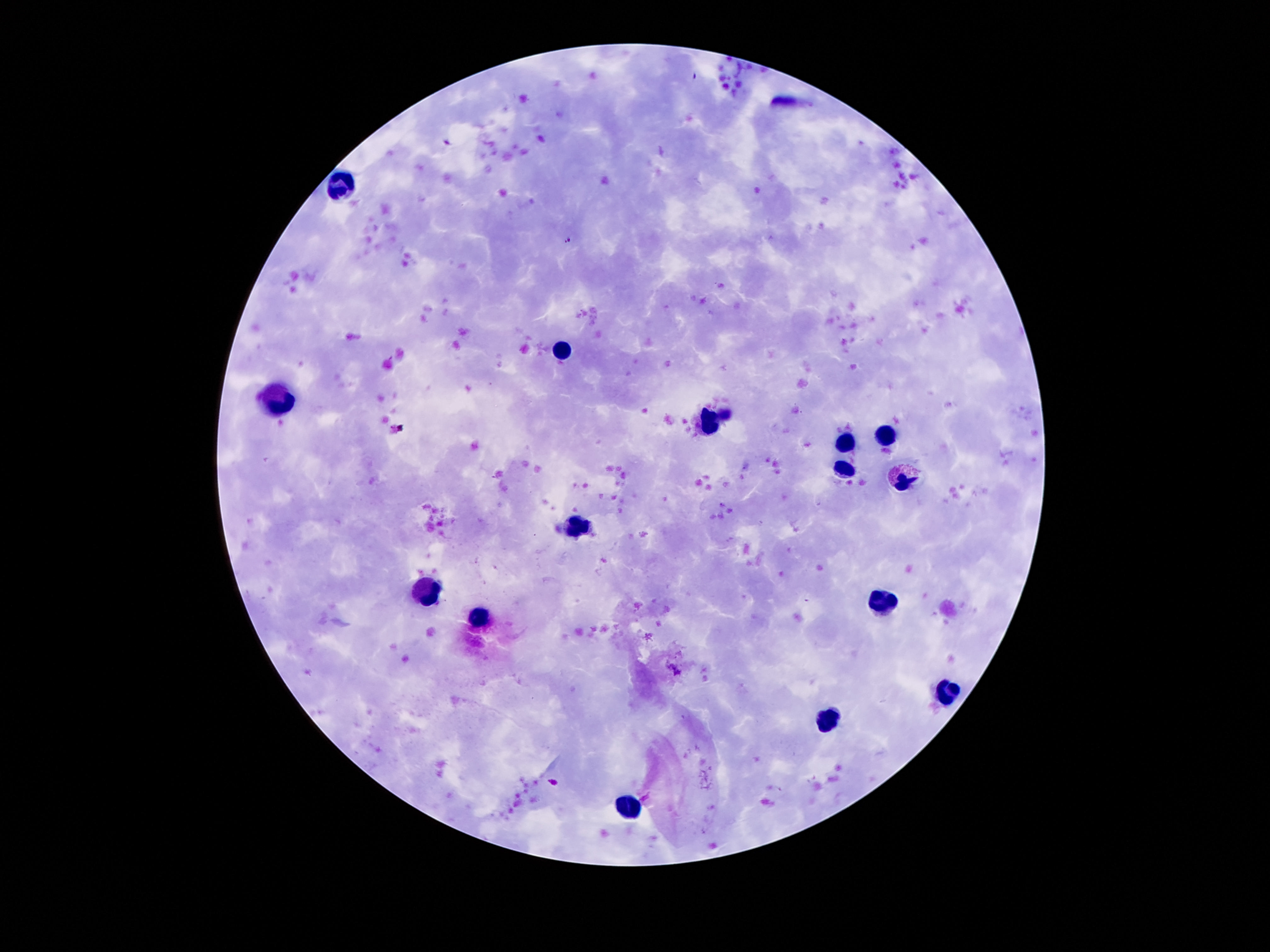
Approximate centers as {x, y} in pixels.
Summary:
  - Leukocyte locations: {343, 184}, {563, 347}, {274, 401}, {712, 418}, {891, 434}, {845, 444}, {841, 468}, {903, 477}, {578, 524}, {425, 595}, {884, 606}, {481, 617}, {944, 692}, {828, 716}, {626, 806}
  - Field of view: one from this slide
  - Image size: 1270×952 pixels
  - Stain: Giemsa
  - Magnification: 100x
  - Patient malaria status: uninfected
  - Preparation: thick blood film
  - Capture: smartphone camera through the microscope eyepiece